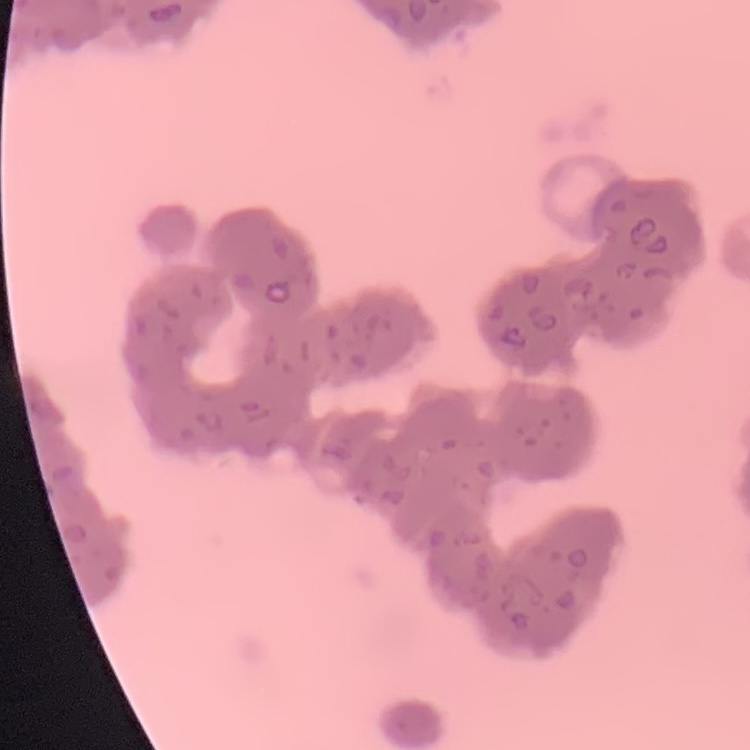

red blood cell morphology = rouleaux formation
stain = Field's or Giemsa
image type = one tile cut from a larger photomicrograph
preparation = thin blood film